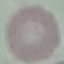

malaria_status: uninfected
preparation: thin smear
image_type: cell patch, automatically extracted from a larger field of view and resized to 64 × 64 pixels
capture: smartphone through the microscope eyepiece
stain: Giemsa